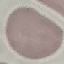
Summary:
  - Malaria status: uninfected
  - Stain: Giemsa
  - Capture: smartphone camera at the microscope eyepiece
  - Preparation: thin smear
  - Image type: automatically extracted cell patch, resized to 64 × 64 pixels